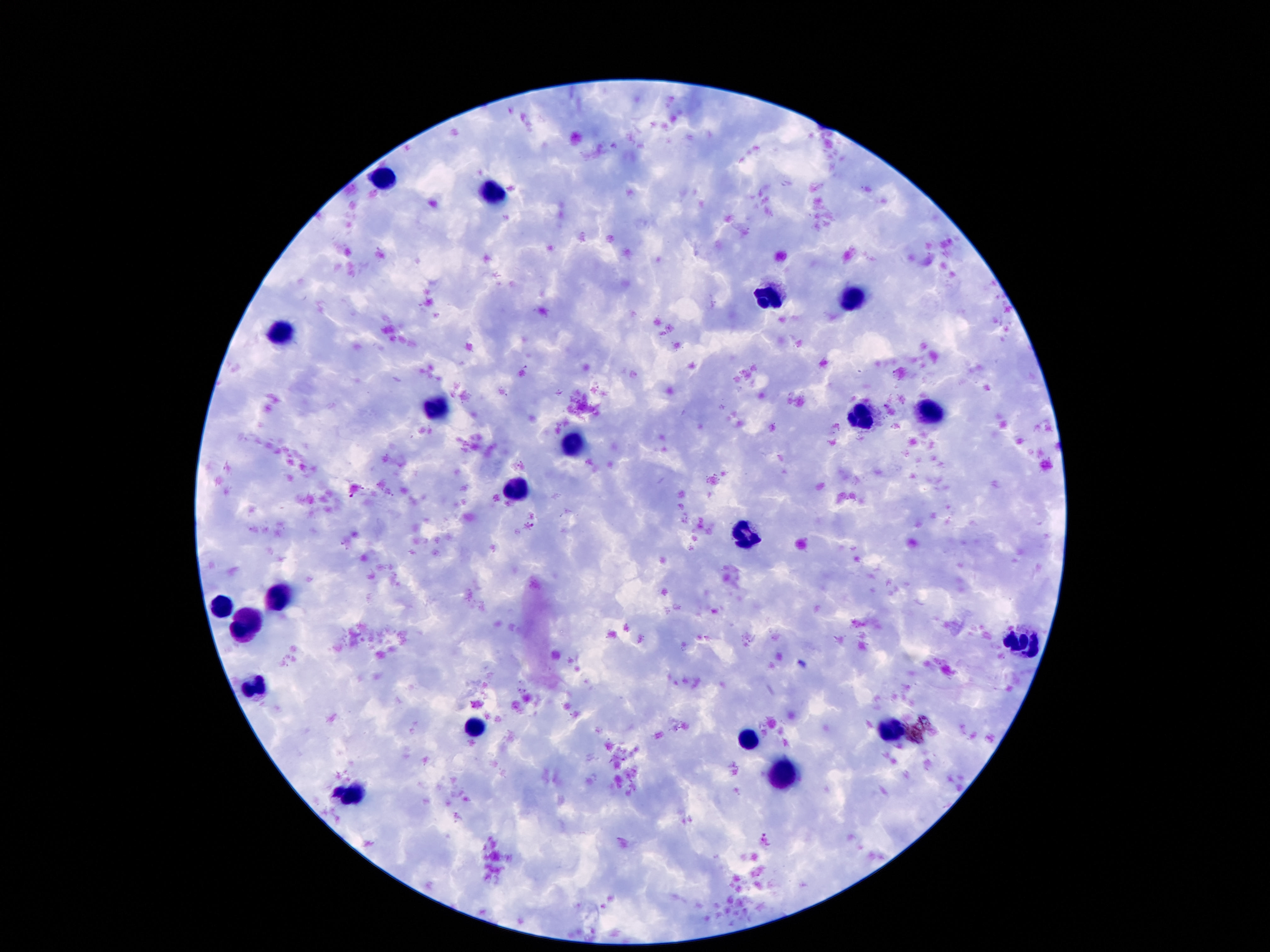

Approximate object centers, in pixels from the top-left corner. Leukocyte locations: (x=382, y=176), (x=493, y=192), (x=852, y=295), (x=770, y=300), (x=284, y=329), (x=439, y=404), (x=932, y=410), (x=859, y=415), (x=573, y=440), (x=521, y=491), (x=745, y=533), (x=282, y=594), (x=221, y=606), (x=250, y=626), (x=1024, y=642), (x=891, y=728), (x=475, y=731), (x=748, y=740), (x=782, y=774), (x=355, y=794). Patient malaria status: negative. Smartphone photograph taken through the microscope eyepiece. 100x magnification. Thick blood film. Image is 1270×952 pixels. Single field of view. Giemsa stain.